Report the malaria status of this cell.
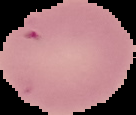
Uninfected.

Image is 136×115 pixels. From a thin blood smear. Segmented cell region on a black background.